Report the malaria status of this cell.
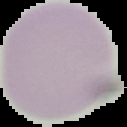
Uninfected.

Cell region segmented out of the field of view; the surrounding area is masked to black. Image is 127×127 pixels. From a thin blood smear.